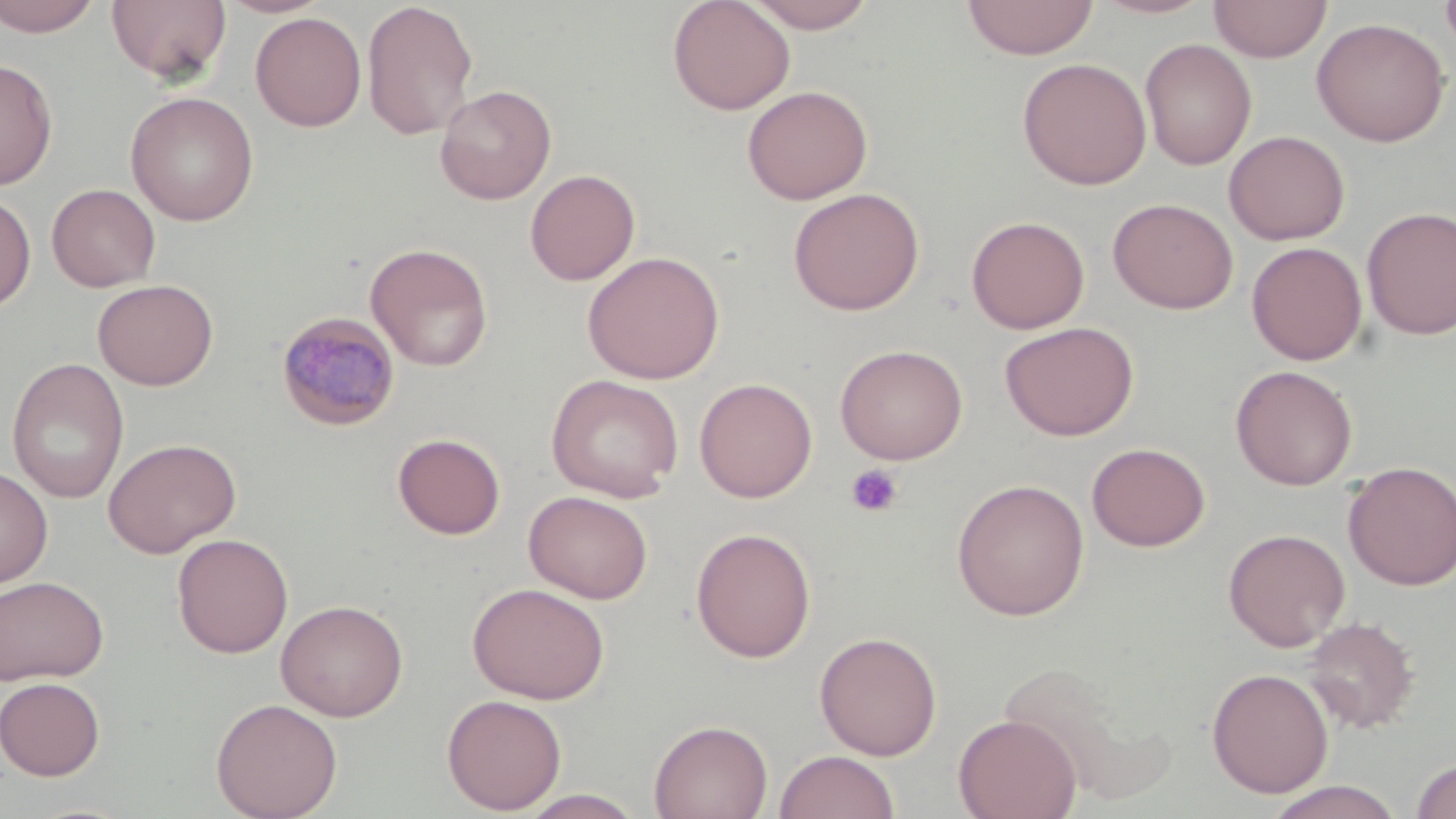
Approximate bounding boxes as (x1, y1, x2, y2) in pixels. Uninfected red blood cell locations: (0, 0, 103, 37), (106, 0, 231, 84), (361, 0, 479, 141), (667, 0, 795, 115), (745, 0, 878, 33), (961, 0, 1099, 60), (1091, 0, 1216, 19), (1440, 0, 1456, 55), (1209, 1, 1332, 62), (250, 12, 366, 131), (1312, 17, 1451, 147), (1139, 38, 1257, 170), (0, 57, 58, 190), (1017, 57, 1152, 190), (434, 84, 557, 204), (742, 85, 872, 205), (125, 91, 260, 226), (1223, 130, 1350, 245), (525, 169, 640, 286), (47, 183, 161, 292), (787, 187, 925, 316), (0, 190, 36, 312), (1108, 197, 1238, 315), (1361, 206, 1456, 340), (966, 215, 1090, 334), (1246, 242, 1367, 365), (365, 243, 493, 371), (582, 251, 724, 384), (92, 278, 218, 390), (1000, 321, 1139, 441), (835, 343, 968, 465), (6, 358, 129, 504), (1230, 365, 1358, 490), (546, 374, 684, 502), (694, 377, 817, 502), (392, 432, 506, 540), (103, 437, 241, 558), (1086, 442, 1211, 551), (1342, 460, 1456, 590), (0, 465, 53, 589), (951, 478, 1090, 621), (524, 490, 653, 604), (690, 527, 816, 663), (1223, 528, 1350, 652), (172, 533, 293, 658), (0, 575, 108, 686), (468, 581, 609, 704), (275, 599, 408, 721), (1302, 616, 1420, 734), (814, 631, 942, 760), (1009, 667, 1161, 801), (1206, 667, 1333, 799), (0, 677, 106, 780), (442, 693, 567, 814), (210, 697, 343, 819), (953, 713, 1081, 819), (649, 719, 773, 819), (774, 750, 899, 819), (1409, 756, 1456, 819), (1263, 781, 1407, 818), (516, 789, 645, 818). Plasmodium malariae-infected red blood cell locations: (276, 311, 402, 432). Platelet locations: (844, 464, 904, 518). Slide-level diagnosis: Plasmodium malariae. Image is 1456×819 pixels. May-Grünwald-Giemsa-stained preparation. Single field of view. Thin blood film. Captured at 1000x magnification. Light microscopy.